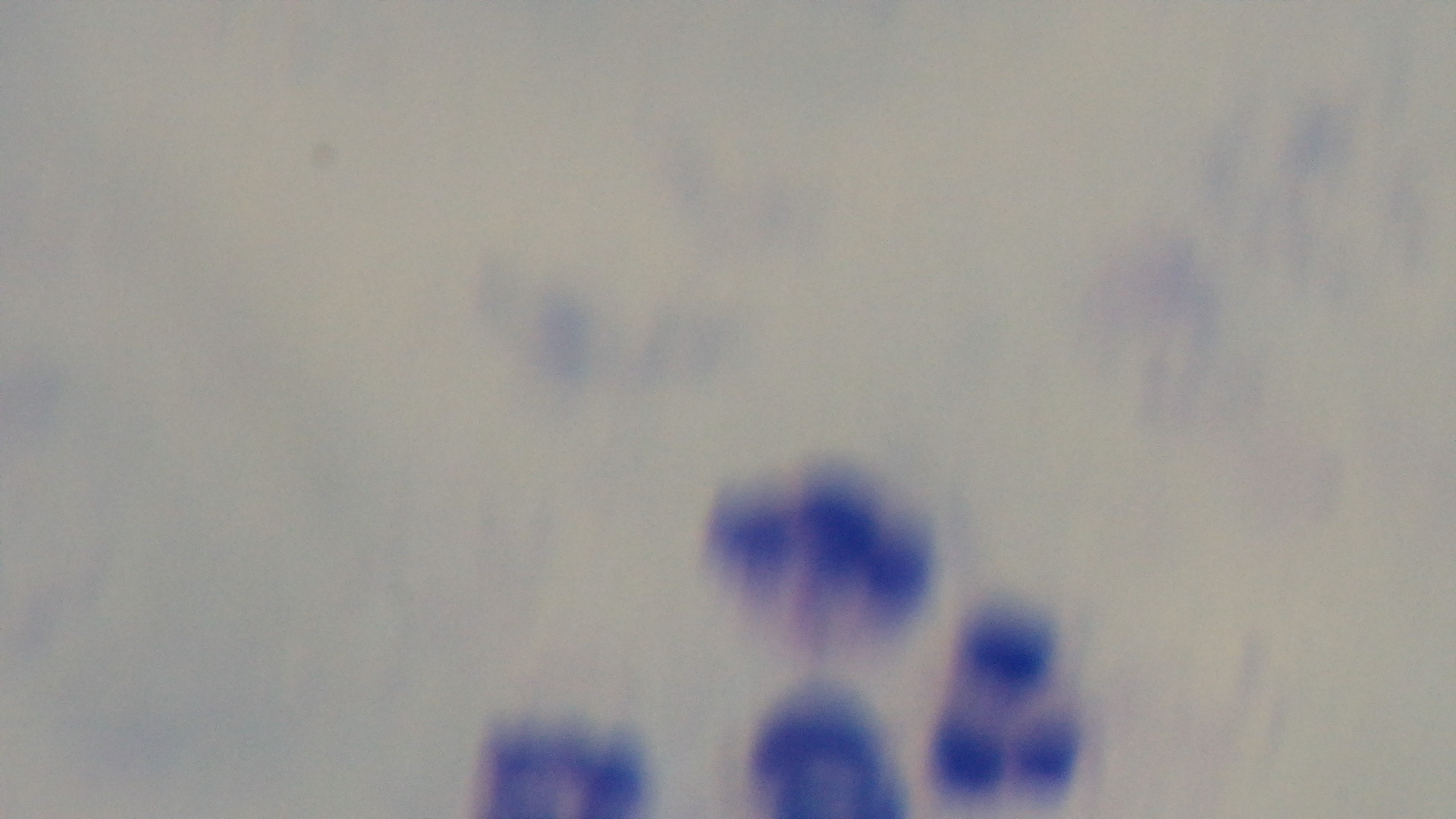

{
  "modality": "light microscopy",
  "objective": "100x oil immersion",
  "malaria_status": "negative",
  "field_of_view": "one from the slide",
  "stain": "Giemsa",
  "capture": "mounted 4K digital camera",
  "preparation": "thick"
}